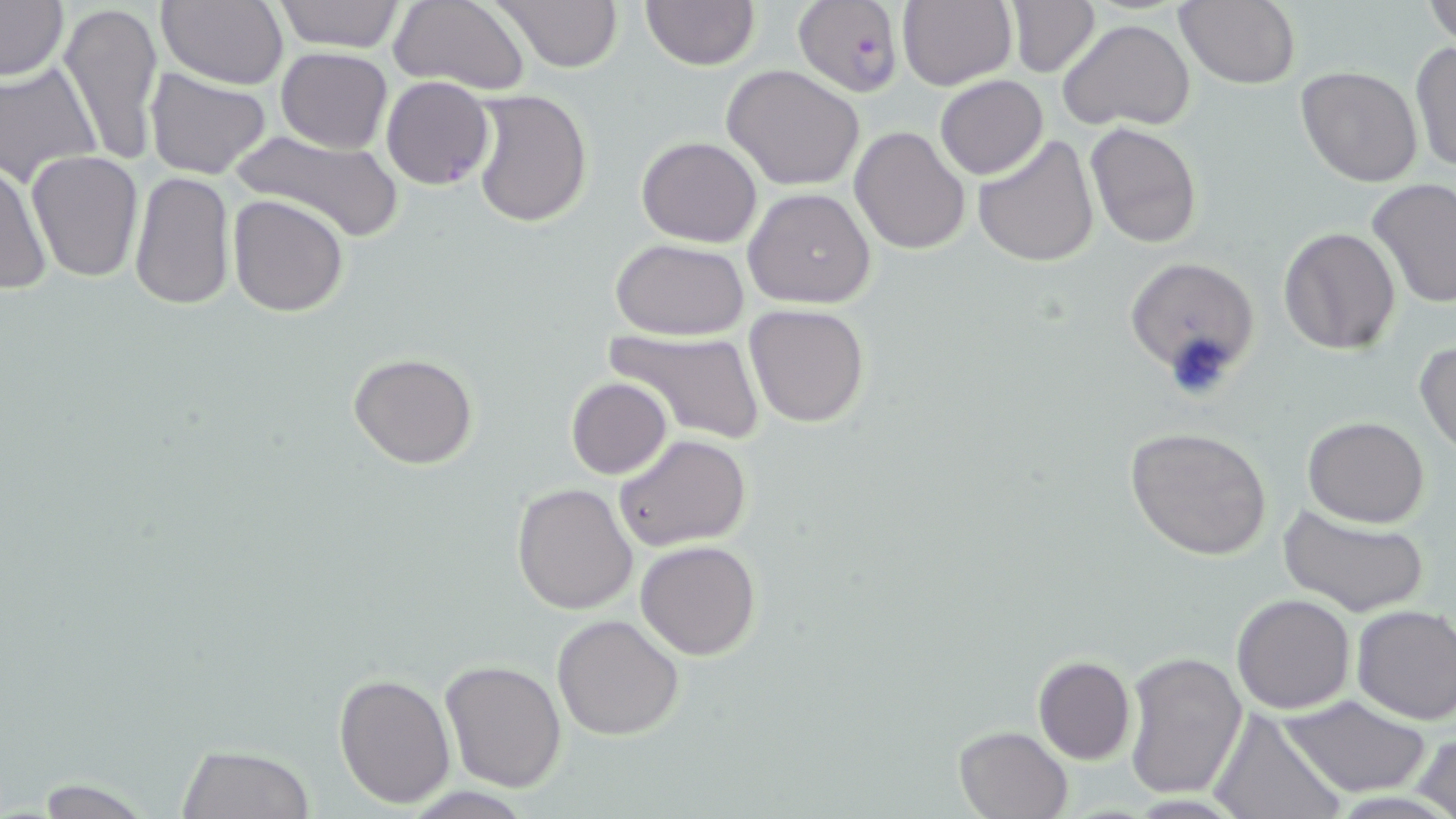

Summary:
  - Coordinate format: approximate bounding boxes as (x1, y1, x2, y2) in pixels
  - Plasmodium falciparum-infected red blood cell locations: (794, 2, 905, 97), (380, 76, 495, 190)
  - Uninfected red blood cell locations: (59, 0, 164, 168), (159, 0, 290, 91), (271, 0, 404, 52), (492, 0, 622, 71), (897, 0, 1017, 93), (1423, 0, 1456, 46), (0, 1, 69, 83), (389, 1, 529, 92), (640, 1, 760, 71), (1174, 1, 1303, 88), (1005, 2, 1101, 77), (1023, 3, 1147, 102), (1057, 19, 1195, 133), (1409, 39, 1456, 176), (274, 47, 392, 153), (0, 62, 101, 187), (723, 64, 865, 191), (1295, 64, 1423, 186), (145, 68, 272, 181), (934, 73, 1048, 180), (470, 89, 592, 227), (1085, 122, 1201, 249), (850, 126, 970, 254), (225, 129, 408, 245), (973, 133, 1098, 269), (636, 136, 763, 246), (26, 150, 144, 282), (0, 156, 51, 297), (127, 170, 235, 311), (1367, 177, 1456, 309), (743, 187, 876, 310), (227, 194, 348, 317), (1278, 226, 1400, 354), (609, 238, 751, 340), (1124, 256, 1261, 386), (744, 303, 870, 427), (605, 326, 767, 445), (1415, 339, 1456, 454), (348, 352, 478, 470), (566, 377, 672, 477), (1304, 416, 1431, 528), (1127, 425, 1274, 561), (613, 433, 751, 551), (512, 482, 639, 615), (1279, 503, 1430, 617), (635, 539, 762, 660), (1231, 593, 1356, 714), (1351, 604, 1456, 725), (552, 614, 684, 740), (1123, 649, 1249, 802), (1032, 655, 1136, 763), (440, 659, 567, 791), (333, 673, 456, 809), (1280, 693, 1432, 798), (1207, 707, 1347, 819), (953, 724, 1073, 818), (1414, 731, 1456, 819), (175, 742, 313, 818), (16, 778, 167, 818)
  - Slide-level diagnosis: Plasmodium falciparum
  - Modality: optical microscopy
  - Field of view: single
  - Magnification: 1000x
  - Preparation: thin blood film
  - Image size: 1456×819 pixels
  - Stain: May-Grünwald-Giemsa